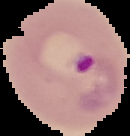

image size = 130×136 pixels
image type = segmented cell region on a black background
result = malaria parasites identified
preparation = thin blood film